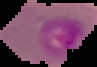
Image is 97×67 pixels. Cell region segmented out of the field of view; the surrounding area is masked to black. Malaria status: parasitized. From a thin blood film.